Give the position of every Plasmodium parasite.
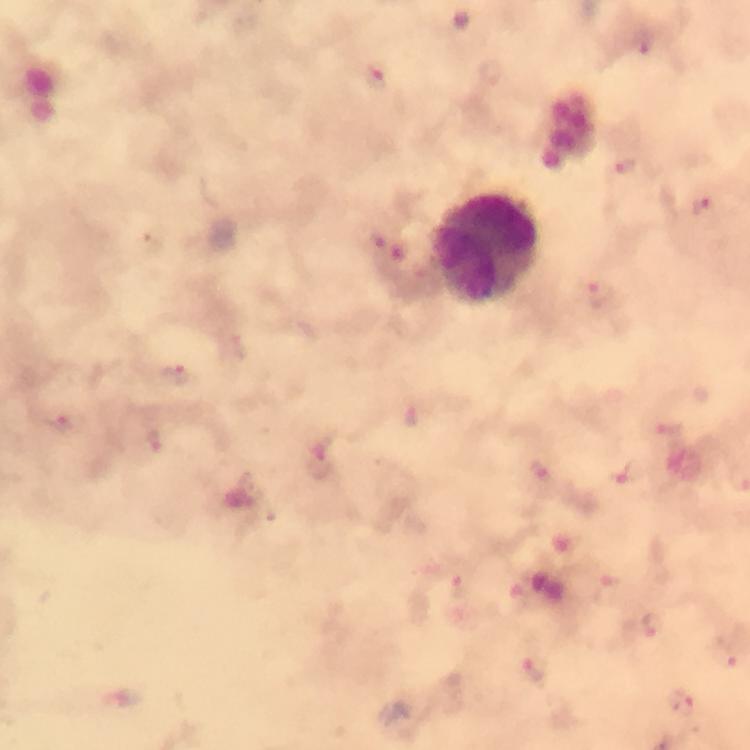

Approximate centers as {x, y} in pixels.
Plasmodium parasites: {643, 41}, {376, 79}, {627, 168}, {703, 208}, {599, 295}, {176, 374}, {411, 417}, {59, 423}, {671, 428}, {154, 443}, {322, 462}, {539, 472}, {456, 585}, {610, 592}, {652, 625}, {728, 657}, {536, 669}, {681, 703}.

Summary:
  - Leukocyte locations: {489, 249}
  - Immersion oil: used
  - Capture: smartphone mounted on the microscope
  - Stain: Giemsa
  - Context: from a malaria diagnostic workup
  - Image size: 750×750 pixels
  - Cropped from: one field of view
  - Preparation: thick blood film
  - Magnification: 100x